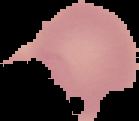
result = no Plasmodium parasites seen
image type = segmented cell region on a black background
preparation = thin blood film
image size = 139×121 pixels